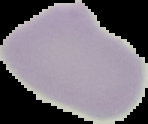 Result: no malaria parasites seen. Image is 148×124 pixels. From a thin blood film. Cell region segmented out of the field of view; the surrounding area is masked to black.